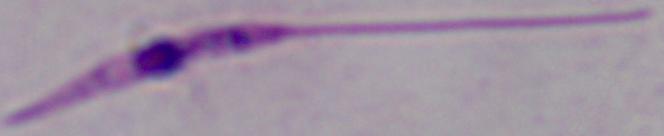

magnification: 1000x
modality: micrograph
identification: Leishmania